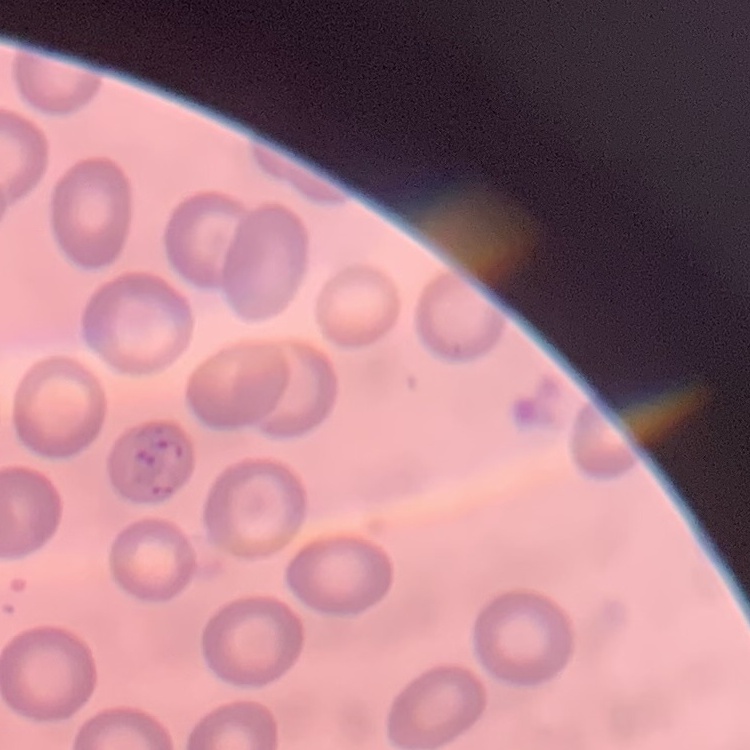
The red blood cells show no rouleaux formation. Square crop of a larger photomicrograph. Thin blood film. Stained with either Field's or Giemsa.